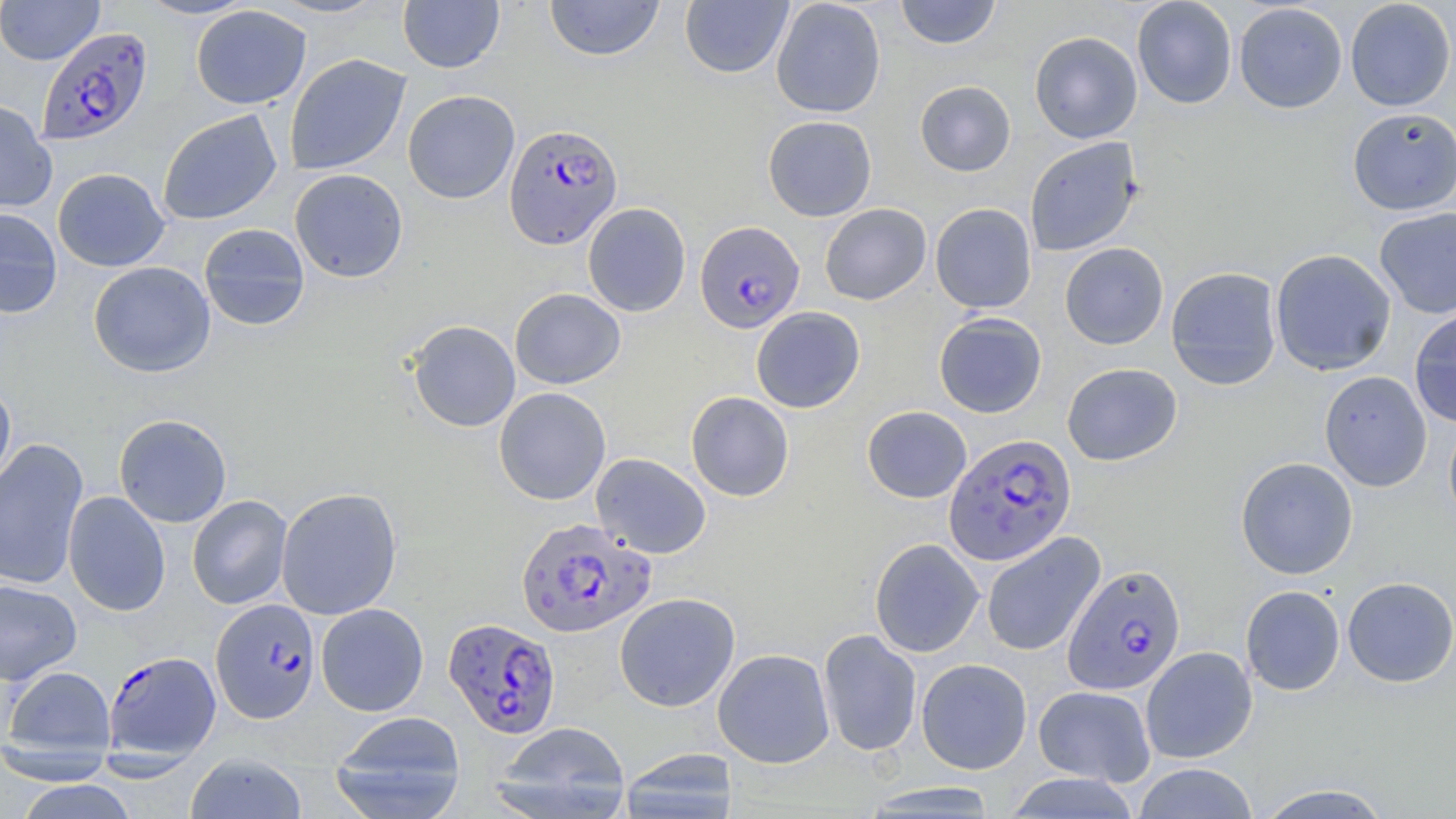
Approximate bounding boxes as (x1, y1, x2, y2) in pixels. Plasmodium falciparum-infected red blood cell locations: (36, 26, 153, 147), (503, 123, 622, 249), (695, 221, 805, 332), (943, 433, 1076, 566), (516, 518, 655, 639), (1062, 563, 1186, 695), (211, 598, 320, 723), (444, 618, 561, 738), (103, 650, 221, 778). Uninfected red blood cell locations: (0, 0, 104, 65), (134, 0, 257, 20), (398, 0, 505, 73), (543, 0, 665, 62), (680, 0, 793, 79), (771, 0, 886, 118), (895, 0, 1001, 49), (1132, 0, 1237, 109), (1345, 0, 1455, 111), (1233, 3, 1347, 114), (191, 5, 311, 109), (1029, 31, 1142, 143), (284, 53, 411, 175), (915, 80, 1016, 176), (402, 89, 520, 204), (0, 99, 57, 213), (1346, 108, 1456, 215), (157, 109, 283, 225), (762, 115, 877, 221), (1024, 137, 1143, 257), (52, 168, 170, 272), (289, 168, 409, 283), (583, 202, 691, 317), (820, 203, 932, 305), (930, 203, 1037, 313), (0, 207, 62, 319), (1374, 207, 1456, 319), (198, 223, 310, 331), (1060, 242, 1169, 349), (1270, 248, 1396, 376), (88, 261, 216, 377), (1165, 266, 1283, 389), (510, 287, 626, 389), (751, 306, 865, 413), (1409, 309, 1456, 427), (933, 312, 1047, 417), (407, 320, 520, 432), (1062, 362, 1182, 466), (1319, 370, 1432, 492), (0, 383, 16, 494), (494, 387, 611, 505), (686, 391, 794, 501), (862, 405, 972, 503), (114, 413, 232, 528), (1444, 413, 1456, 532), (0, 438, 89, 591), (590, 452, 711, 559), (1235, 457, 1358, 579), (276, 486, 403, 620), (62, 491, 171, 616), (187, 495, 292, 609), (981, 532, 1105, 657), (869, 538, 984, 658), (1342, 576, 1456, 687), (0, 579, 82, 684), (1241, 585, 1345, 695), (614, 592, 740, 712), (316, 603, 429, 716), (818, 629, 922, 757), (1140, 646, 1257, 763), (713, 648, 835, 768), (916, 658, 1032, 774), (2, 666, 116, 762), (1033, 685, 1156, 786), (328, 711, 467, 819), (494, 721, 631, 818), (618, 748, 739, 819), (185, 752, 307, 819), (1132, 762, 1259, 819), (13, 780, 142, 819), (859, 782, 1002, 816), (1252, 783, 1398, 818). Slide-level diagnosis: Plasmodium falciparum. May-Grünwald-Giemsa stain. Optical microscopy. Single field of view. Thin blood film. Captured at 1000x magnification. Image is 1456×819 pixels.